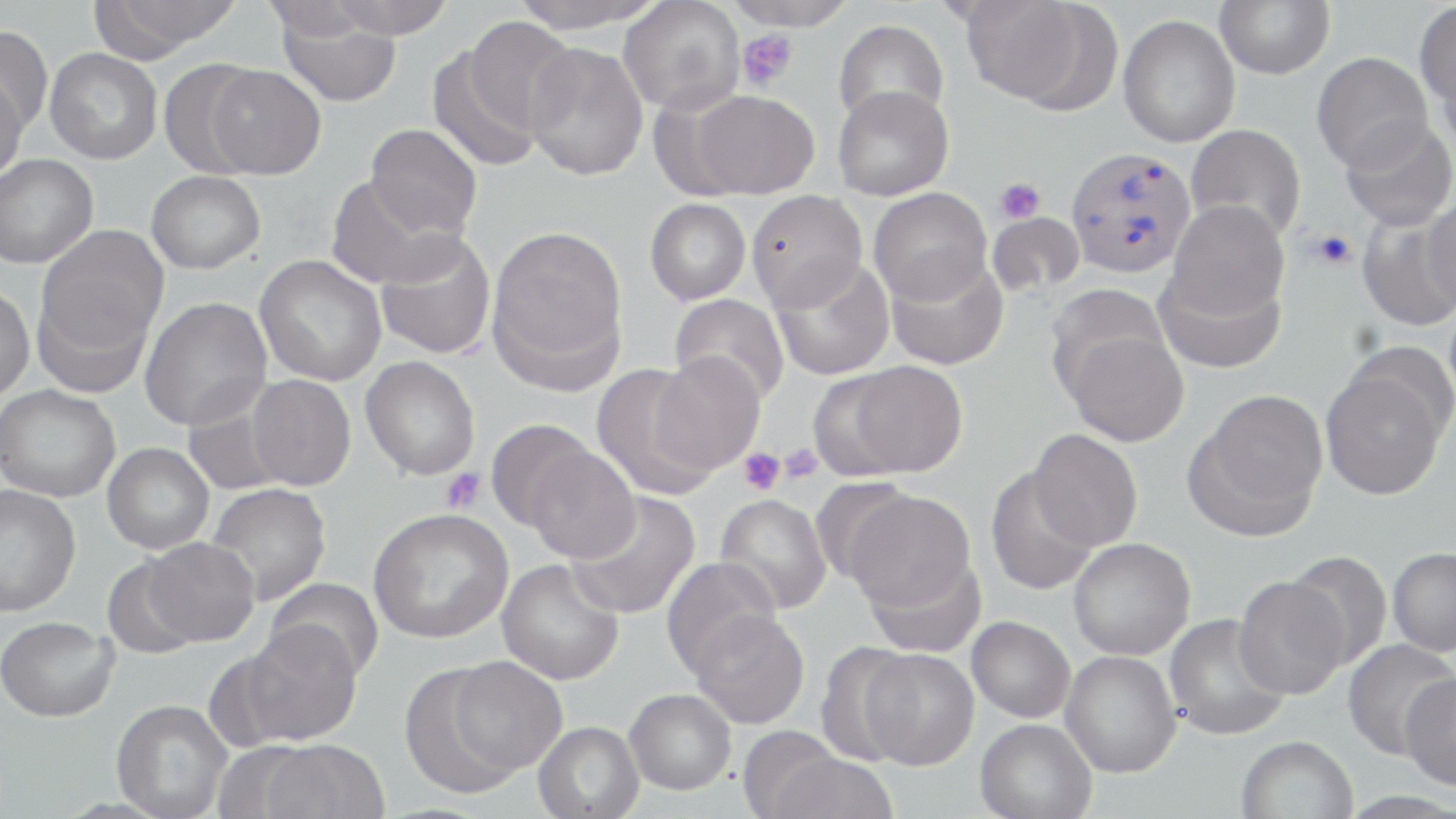
{
  "slide_level_diagnosis": "Plasmodium vivax",
  "platelet_locations": "approximate bounding boxes as named x1/y1/x2/y2 corners in pixels: (x1=737, y1=28, x2=798, y2=91), (x1=996, y1=177, x2=1045, y2=224), (x1=1308, y1=229, x2=1356, y2=270), (x1=777, y1=442, x2=825, y2=484), (x1=738, y1=447, x2=785, y2=495), (x1=440, y1=468, x2=487, y2=514)",
  "modality": "light microscopy",
  "image_size": "1456×819 pixels",
  "field_of_view": "one of a larger specimen",
  "plasmodium_vivax_infected_red_blood_cell_locations": "approximate bounding boxes as named x1/y1/x2/y2 corners in pixels: (x1=1065, y1=146, x2=1196, y2=278)",
  "stain": "May-Grünwald-Giemsa",
  "magnification": "1000x",
  "uninfected_red_blood_cell_locations": "approximate bounding boxes as named x1/y1/x2/y2 corners in pixels: (x1=92, y1=0, x2=243, y2=58), (x1=327, y1=0, x2=456, y2=38), (x1=508, y1=0, x2=667, y2=34), (x1=724, y1=0, x2=860, y2=30), (x1=959, y1=0, x2=1107, y2=110), (x1=1215, y1=0, x2=1335, y2=79), (x1=618, y1=1, x2=745, y2=114), (x1=1414, y1=3, x2=1456, y2=110), (x1=274, y1=10, x2=402, y2=107), (x1=1118, y1=14, x2=1240, y2=148), (x1=464, y1=17, x2=578, y2=136), (x1=833, y1=19, x2=949, y2=129), (x1=0, y1=25, x2=54, y2=137), (x1=523, y1=43, x2=648, y2=181), (x1=427, y1=45, x2=542, y2=174), (x1=45, y1=48, x2=163, y2=164), (x1=1311, y1=52, x2=1433, y2=172), (x1=158, y1=60, x2=267, y2=178), (x1=205, y1=65, x2=326, y2=179), (x1=0, y1=74, x2=27, y2=184), (x1=833, y1=85, x2=954, y2=201), (x1=688, y1=90, x2=819, y2=198), (x1=1339, y1=117, x2=1456, y2=231), (x1=365, y1=124, x2=482, y2=238), (x1=1186, y1=124, x2=1307, y2=243), (x1=0, y1=154, x2=98, y2=268), (x1=146, y1=171, x2=265, y2=273), (x1=325, y1=174, x2=462, y2=289), (x1=869, y1=188, x2=992, y2=305), (x1=746, y1=190, x2=868, y2=311), (x1=1422, y1=194, x2=1456, y2=316), (x1=645, y1=198, x2=751, y2=305), (x1=1167, y1=200, x2=1290, y2=321), (x1=987, y1=212, x2=1085, y2=298), (x1=1356, y1=212, x2=1456, y2=332), (x1=35, y1=225, x2=170, y2=364), (x1=486, y1=226, x2=629, y2=389), (x1=373, y1=229, x2=496, y2=360), (x1=885, y1=253, x2=1008, y2=371), (x1=254, y1=255, x2=387, y2=386), (x1=770, y1=257, x2=895, y2=381), (x1=1155, y1=263, x2=1286, y2=374), (x1=32, y1=279, x2=158, y2=401), (x1=0, y1=284, x2=35, y2=403), (x1=669, y1=294, x2=790, y2=406), (x1=140, y1=297, x2=273, y2=431), (x1=1060, y1=327, x2=1189, y2=447), (x1=650, y1=352, x2=764, y2=475), (x1=361, y1=357, x2=480, y2=481), (x1=831, y1=361, x2=969, y2=479), (x1=1320, y1=361, x2=1450, y2=501), (x1=591, y1=364, x2=719, y2=501), (x1=245, y1=375, x2=356, y2=491), (x1=0, y1=384, x2=121, y2=502), (x1=1187, y1=390, x2=1328, y2=538), (x1=183, y1=392, x2=290, y2=496), (x1=485, y1=421, x2=601, y2=535), (x1=1028, y1=429, x2=1143, y2=551), (x1=102, y1=443, x2=214, y2=554), (x1=523, y1=447, x2=639, y2=563), (x1=985, y1=467, x2=1100, y2=596), (x1=206, y1=483, x2=332, y2=606), (x1=0, y1=485, x2=81, y2=616), (x1=565, y1=491, x2=701, y2=620), (x1=843, y1=491, x2=975, y2=611), (x1=714, y1=494, x2=832, y2=615), (x1=368, y1=508, x2=513, y2=643), (x1=143, y1=537, x2=259, y2=645), (x1=1068, y1=538, x2=1196, y2=659), (x1=1387, y1=547, x2=1456, y2=657), (x1=1285, y1=550, x2=1392, y2=670), (x1=863, y1=553, x2=987, y2=658), (x1=101, y1=556, x2=207, y2=659), (x1=662, y1=557, x2=782, y2=678), (x1=496, y1=559, x2=624, y2=685), (x1=1233, y1=575, x2=1350, y2=699), (x1=263, y1=577, x2=384, y2=682), (x1=688, y1=608, x2=810, y2=728), (x1=1163, y1=613, x2=1291, y2=740), (x1=0, y1=616, x2=117, y2=722), (x1=967, y1=616, x2=1076, y2=723), (x1=236, y1=622, x2=362, y2=746), (x1=1342, y1=639, x2=1455, y2=760), (x1=814, y1=641, x2=921, y2=766), (x1=858, y1=648, x2=979, y2=769), (x1=1060, y1=651, x2=1181, y2=778), (x1=447, y1=656, x2=566, y2=775), (x1=400, y1=660, x2=535, y2=799), (x1=1400, y1=673, x2=1456, y2=791), (x1=625, y1=689, x2=736, y2=794), (x1=111, y1=699, x2=233, y2=819), (x1=975, y1=719, x2=1097, y2=819), (x1=533, y1=720, x2=645, y2=819), (x1=736, y1=726, x2=847, y2=818), (x1=1236, y1=734, x2=1359, y2=819), (x1=256, y1=739, x2=390, y2=819), (x1=767, y1=752, x2=899, y2=819)",
  "preparation": "thin blood smear"
}